Outline platelets.
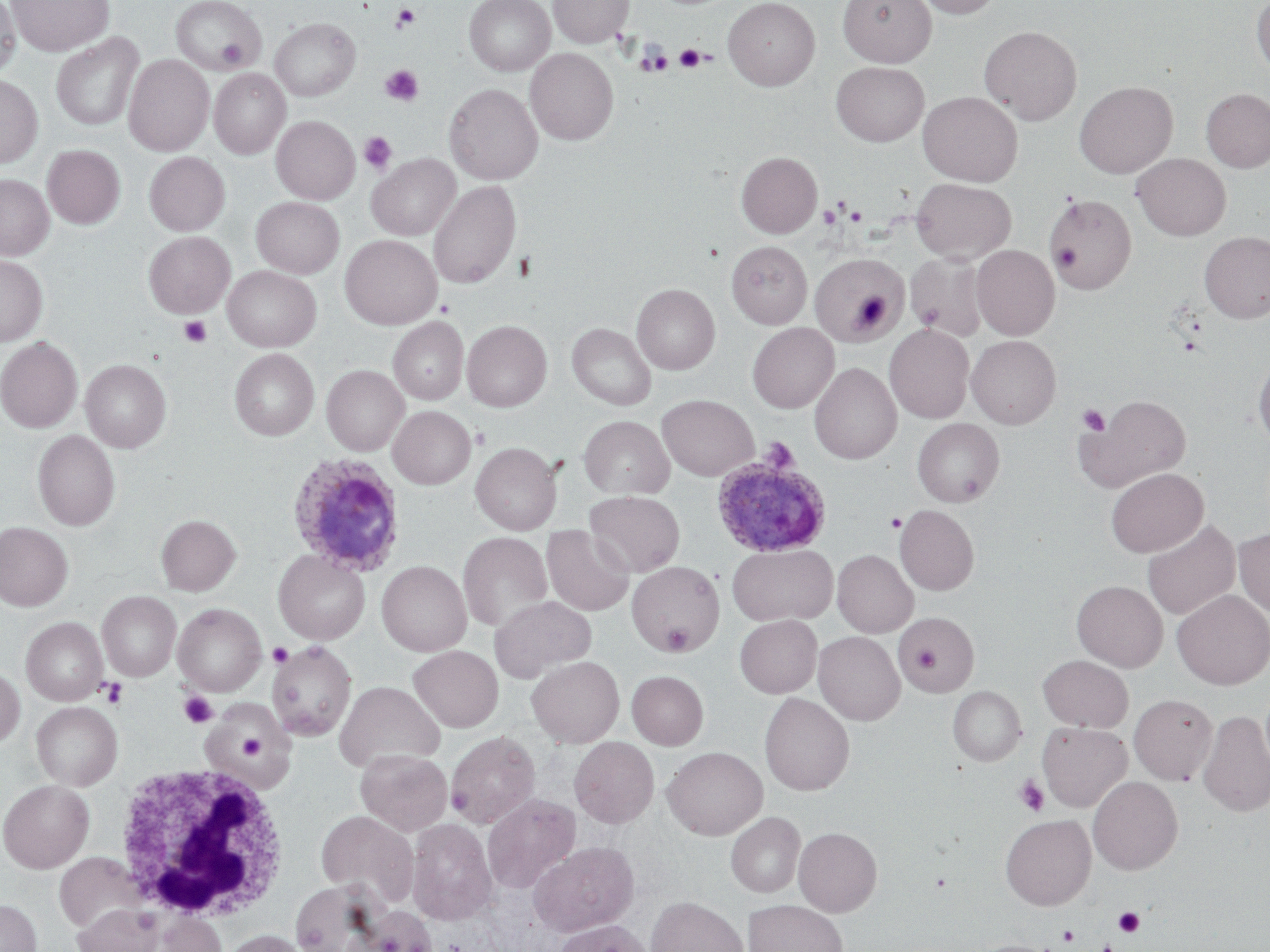

Approximate bounding boxes as named x1/y1/x2/y2 corners in pixels.
Platelets: (x1=392, y1=3, x2=420, y2=32), (x1=217, y1=38, x2=251, y2=68), (x1=674, y1=44, x2=707, y2=72), (x1=639, y1=48, x2=671, y2=75), (x1=380, y1=66, x2=422, y2=106), (x1=359, y1=132, x2=397, y2=174), (x1=820, y1=206, x2=842, y2=228), (x1=844, y1=206, x2=867, y2=226), (x1=1052, y1=245, x2=1081, y2=271), (x1=851, y1=293, x2=891, y2=327), (x1=914, y1=300, x2=943, y2=328), (x1=179, y1=316, x2=212, y2=347), (x1=1077, y1=403, x2=1110, y2=436), (x1=886, y1=512, x2=906, y2=532), (x1=661, y1=621, x2=694, y2=654), (x1=268, y1=642, x2=293, y2=667), (x1=911, y1=646, x2=941, y2=673), (x1=99, y1=678, x2=127, y2=708), (x1=179, y1=691, x2=218, y2=728), (x1=234, y1=730, x2=268, y2=765), (x1=1014, y1=776, x2=1049, y2=815), (x1=448, y1=786, x2=474, y2=816), (x1=1113, y1=907, x2=1144, y2=936), (x1=1058, y1=925, x2=1079, y2=945), (x1=1099, y1=940, x2=1117, y2=952).

Uninfected red blood cell locations: (x1=0, y1=0, x2=22, y2=79), (x1=6, y1=0, x2=113, y2=55), (x1=171, y1=0, x2=266, y2=74), (x1=464, y1=0, x2=555, y2=76), (x1=549, y1=0, x2=633, y2=47), (x1=723, y1=0, x2=821, y2=90), (x1=838, y1=0, x2=936, y2=67), (x1=914, y1=0, x2=1002, y2=18), (x1=1251, y1=0, x2=1270, y2=76), (x1=269, y1=18, x2=360, y2=101), (x1=979, y1=25, x2=1083, y2=125), (x1=51, y1=33, x2=144, y2=131), (x1=526, y1=48, x2=617, y2=145), (x1=124, y1=54, x2=213, y2=156), (x1=831, y1=62, x2=929, y2=146), (x1=209, y1=68, x2=290, y2=159), (x1=0, y1=75, x2=42, y2=168), (x1=1074, y1=81, x2=1177, y2=178), (x1=444, y1=83, x2=543, y2=184), (x1=1200, y1=88, x2=1270, y2=172), (x1=918, y1=91, x2=1023, y2=186), (x1=271, y1=116, x2=360, y2=204), (x1=42, y1=144, x2=125, y2=229), (x1=144, y1=152, x2=229, y2=236), (x1=736, y1=152, x2=822, y2=238), (x1=366, y1=153, x2=461, y2=240), (x1=1132, y1=153, x2=1231, y2=240), (x1=0, y1=174, x2=54, y2=260), (x1=911, y1=178, x2=1016, y2=263), (x1=428, y1=180, x2=522, y2=289), (x1=1046, y1=194, x2=1136, y2=293), (x1=251, y1=197, x2=344, y2=278), (x1=143, y1=231, x2=234, y2=318), (x1=1199, y1=231, x2=1270, y2=323), (x1=340, y1=235, x2=441, y2=329), (x1=727, y1=241, x2=812, y2=329), (x1=972, y1=246, x2=1059, y2=339), (x1=906, y1=253, x2=989, y2=340), (x1=0, y1=254, x2=48, y2=347), (x1=811, y1=254, x2=906, y2=344), (x1=222, y1=266, x2=321, y2=351), (x1=632, y1=284, x2=719, y2=374), (x1=388, y1=317, x2=469, y2=405), (x1=462, y1=320, x2=552, y2=411), (x1=567, y1=323, x2=656, y2=410), (x1=747, y1=323, x2=838, y2=413), (x1=885, y1=324, x2=973, y2=423), (x1=967, y1=335, x2=1061, y2=428), (x1=0, y1=337, x2=83, y2=432), (x1=229, y1=349, x2=319, y2=440), (x1=1253, y1=350, x2=1270, y2=448), (x1=80, y1=359, x2=171, y2=452), (x1=810, y1=362, x2=902, y2=464), (x1=322, y1=365, x2=409, y2=455), (x1=657, y1=394, x2=759, y2=480), (x1=1081, y1=394, x2=1191, y2=491), (x1=388, y1=406, x2=476, y2=489), (x1=579, y1=416, x2=674, y2=498), (x1=912, y1=418, x2=1004, y2=507), (x1=33, y1=429, x2=120, y2=531), (x1=471, y1=442, x2=562, y2=535), (x1=1105, y1=468, x2=1208, y2=557), (x1=585, y1=491, x2=685, y2=577), (x1=895, y1=504, x2=978, y2=595), (x1=156, y1=514, x2=241, y2=595), (x1=1142, y1=519, x2=1241, y2=620), (x1=0, y1=522, x2=73, y2=611), (x1=542, y1=526, x2=635, y2=616), (x1=1234, y1=528, x2=1270, y2=617), (x1=458, y1=532, x2=553, y2=632), (x1=727, y1=544, x2=837, y2=626), (x1=833, y1=549, x2=918, y2=637), (x1=273, y1=550, x2=370, y2=644), (x1=377, y1=561, x2=472, y2=656), (x1=627, y1=561, x2=724, y2=655), (x1=1072, y1=580, x2=1168, y2=672), (x1=1172, y1=590, x2=1270, y2=689), (x1=97, y1=591, x2=181, y2=681), (x1=490, y1=595, x2=597, y2=682), (x1=173, y1=603, x2=266, y2=695), (x1=897, y1=611, x2=979, y2=695), (x1=734, y1=615, x2=822, y2=698), (x1=21, y1=617, x2=107, y2=706), (x1=814, y1=631, x2=905, y2=725), (x1=266, y1=641, x2=356, y2=741), (x1=408, y1=645, x2=503, y2=731), (x1=1038, y1=655, x2=1133, y2=731), (x1=527, y1=656, x2=625, y2=746), (x1=0, y1=665, x2=25, y2=748), (x1=627, y1=671, x2=708, y2=750), (x1=335, y1=680, x2=444, y2=772), (x1=948, y1=686, x2=1026, y2=765), (x1=759, y1=693, x2=854, y2=796), (x1=1129, y1=694, x2=1217, y2=785), (x1=31, y1=701, x2=122, y2=790), (x1=203, y1=705, x2=293, y2=787), (x1=1198, y1=710, x2=1270, y2=817), (x1=1038, y1=721, x2=1132, y2=812), (x1=446, y1=731, x2=541, y2=828), (x1=570, y1=737, x2=659, y2=828), (x1=662, y1=746, x2=768, y2=839), (x1=355, y1=749, x2=451, y2=835), (x1=1088, y1=776, x2=1183, y2=874), (x1=0, y1=779, x2=94, y2=872), (x1=482, y1=794, x2=581, y2=893), (x1=315, y1=810, x2=419, y2=907), (x1=726, y1=812, x2=805, y2=897), (x1=1000, y1=814, x2=1096, y2=910), (x1=406, y1=818, x2=498, y2=925), (x1=794, y1=826, x2=882, y2=916), (x1=529, y1=840, x2=639, y2=936), (x1=54, y1=853, x2=147, y2=934), (x1=290, y1=881, x2=384, y2=952), (x1=645, y1=896, x2=749, y2=952), (x1=0, y1=899, x2=42, y2=952), (x1=743, y1=899, x2=848, y2=952), (x1=72, y1=903, x2=162, y2=952), (x1=347, y1=905, x2=438, y2=952), (x1=155, y1=911, x2=226, y2=952), (x1=551, y1=919, x2=652, y2=952), (x1=220, y1=929, x2=313, y2=952). White blood cell locations: (x1=114, y1=764, x2=294, y2=922). Plasmodium ovale-infected red blood cell locations: (x1=710, y1=452, x2=833, y2=557), (x1=286, y1=453, x2=407, y2=576). Slide-level diagnosis: Plasmodium ovale. Single field of view. Captured at 1000x magnification. Thin blood smear. May-Grünwald-Giemsa-stained preparation. Image is 1270×952 pixels. Optical microscopy.